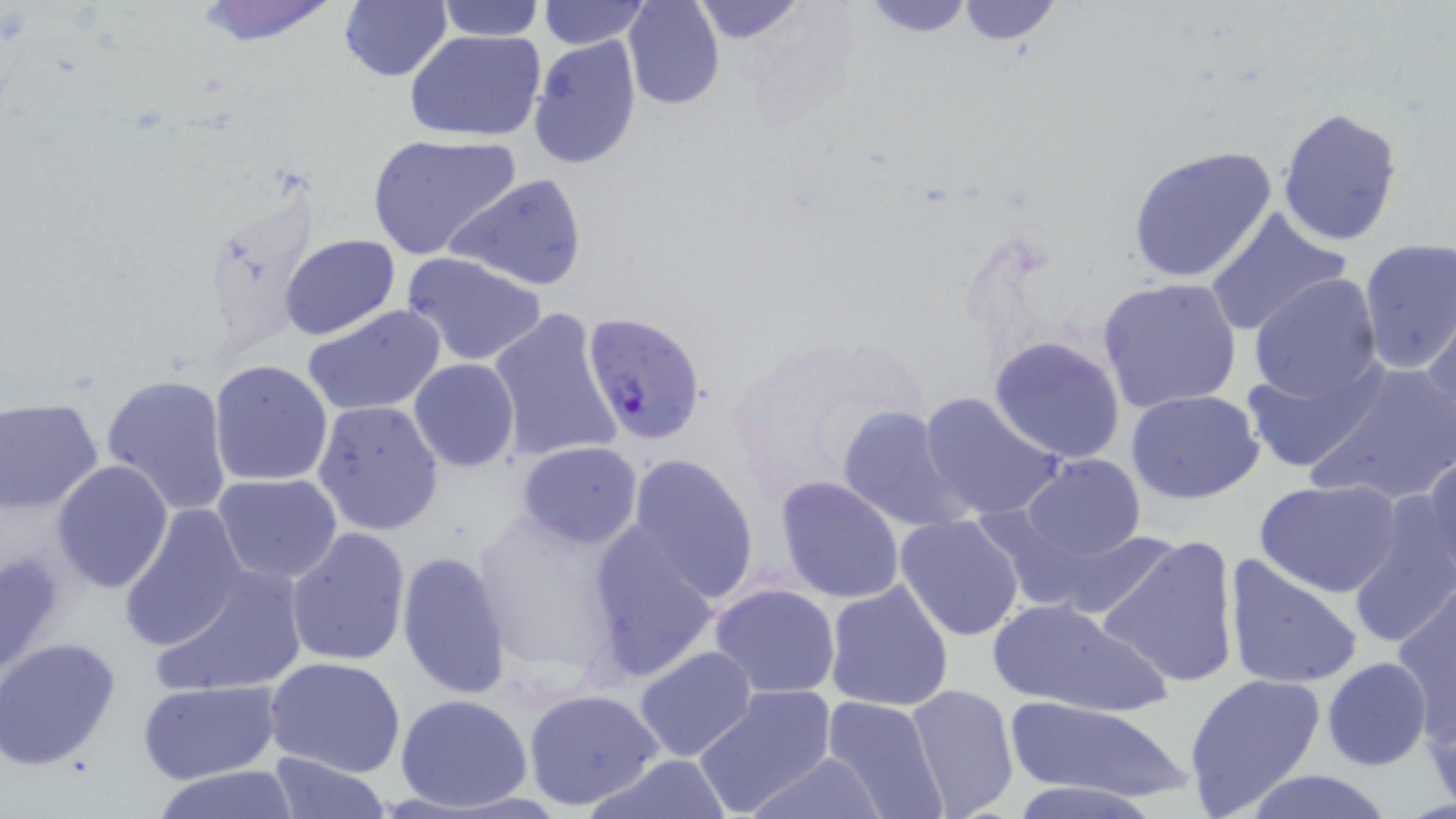

slide-level diagnosis = Plasmodium falciparum
preparation = thin blood film
image size = 1456×819 pixels
modality = optical microscopy
field of view = one of a larger specimen
Plasmodium falciparum-infected red blood cell locations = approximate bounding boxes as named x1/y1/x2/y2 corners in pixels: (x1=582, y1=313, x2=708, y2=445)
magnification = 1000x
uninfected red blood cell locations = approximate bounding boxes as named x1/y1/x2/y2 corners in pixels: (x1=187, y1=0, x2=343, y2=48), (x1=338, y1=0, x2=452, y2=82), (x1=539, y1=0, x2=648, y2=50), (x1=624, y1=0, x2=726, y2=110), (x1=687, y1=0, x2=808, y2=45), (x1=856, y1=0, x2=979, y2=38), (x1=954, y1=0, x2=1064, y2=47), (x1=436, y1=1, x2=544, y2=41), (x1=405, y1=28, x2=547, y2=142), (x1=527, y1=35, x2=642, y2=170), (x1=1277, y1=107, x2=1404, y2=248), (x1=367, y1=133, x2=521, y2=261), (x1=1126, y1=143, x2=1281, y2=286), (x1=445, y1=172, x2=590, y2=293), (x1=1203, y1=207, x2=1352, y2=339), (x1=280, y1=234, x2=401, y2=340), (x1=1356, y1=237, x2=1456, y2=374), (x1=402, y1=252, x2=549, y2=367), (x1=1247, y1=274, x2=1383, y2=404), (x1=1096, y1=275, x2=1245, y2=414), (x1=303, y1=305, x2=447, y2=417), (x1=488, y1=306, x2=621, y2=464), (x1=1421, y1=316, x2=1455, y2=452), (x1=725, y1=333, x2=929, y2=512), (x1=988, y1=334, x2=1128, y2=464), (x1=1239, y1=356, x2=1390, y2=475), (x1=208, y1=358, x2=334, y2=488), (x1=408, y1=359, x2=520, y2=472), (x1=1304, y1=361, x2=1456, y2=507), (x1=100, y1=374, x2=234, y2=515), (x1=1124, y1=390, x2=1266, y2=505), (x1=916, y1=391, x2=1062, y2=524), (x1=0, y1=396, x2=104, y2=515), (x1=311, y1=400, x2=444, y2=537), (x1=837, y1=406, x2=973, y2=534), (x1=516, y1=441, x2=644, y2=550), (x1=622, y1=452, x2=760, y2=602), (x1=1414, y1=453, x2=1456, y2=581), (x1=1018, y1=454, x2=1146, y2=562), (x1=51, y1=460, x2=175, y2=593), (x1=212, y1=473, x2=343, y2=585), (x1=774, y1=476, x2=906, y2=604), (x1=1255, y1=479, x2=1403, y2=598), (x1=1350, y1=494, x2=1455, y2=647), (x1=118, y1=501, x2=251, y2=654), (x1=468, y1=508, x2=632, y2=678), (x1=895, y1=515, x2=1026, y2=642), (x1=583, y1=523, x2=721, y2=683), (x1=286, y1=527, x2=411, y2=666), (x1=1097, y1=533, x2=1242, y2=690), (x1=0, y1=545, x2=70, y2=680), (x1=396, y1=550, x2=513, y2=700), (x1=1223, y1=554, x2=1363, y2=691), (x1=150, y1=561, x2=308, y2=699), (x1=823, y1=580, x2=955, y2=713), (x1=708, y1=583, x2=841, y2=697), (x1=1391, y1=587, x2=1456, y2=743), (x1=987, y1=597, x2=1169, y2=714), (x1=0, y1=637, x2=122, y2=771), (x1=633, y1=645, x2=759, y2=765), (x1=265, y1=655, x2=407, y2=776), (x1=1322, y1=657, x2=1433, y2=771), (x1=1183, y1=671, x2=1326, y2=816), (x1=136, y1=680, x2=279, y2=784), (x1=906, y1=683, x2=1019, y2=817), (x1=692, y1=687, x2=836, y2=817), (x1=522, y1=688, x2=665, y2=812), (x1=1423, y1=689, x2=1456, y2=809), (x1=394, y1=692, x2=534, y2=810), (x1=821, y1=695, x2=948, y2=819), (x1=1002, y1=698, x2=1196, y2=806), (x1=265, y1=751, x2=392, y2=819), (x1=749, y1=751, x2=887, y2=818), (x1=586, y1=753, x2=735, y2=819), (x1=148, y1=766, x2=300, y2=819), (x1=1235, y1=769, x2=1401, y2=819), (x1=1006, y1=782, x2=1161, y2=819)
stain = May-Grünwald-Giemsa